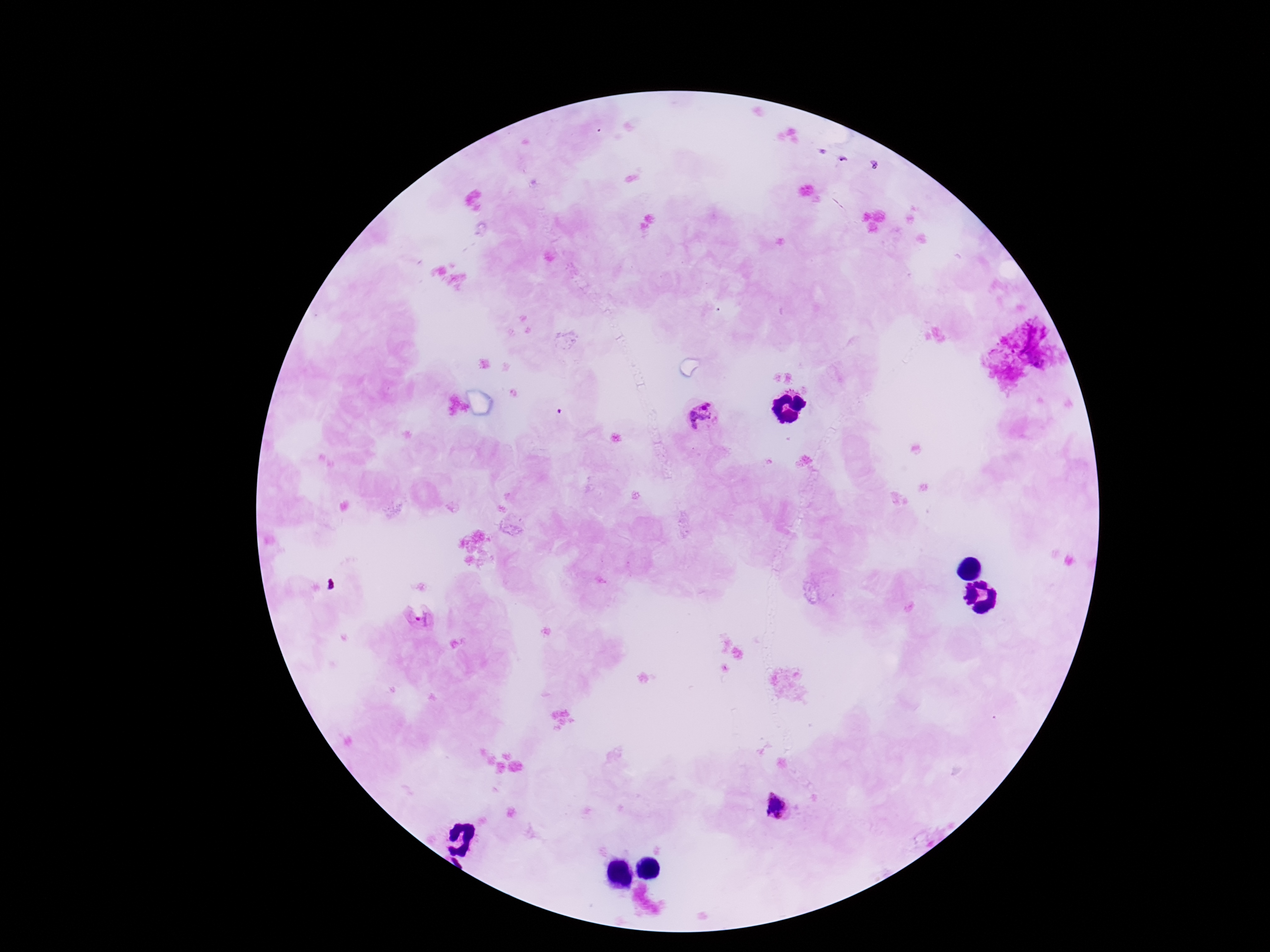

field of view = single
preparation = thick peripheral-blood smear
stain = Giemsa
capture = smartphone camera through the microscope eyepiece
image size = 1270×952 pixels
magnification = 100x
Plasmodium parasite locations = approximate centers as {x, y} in pixels: {703, 418}, {421, 619}, {779, 807}
patient malaria status = positive